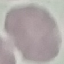

{
  "malaria_status": "uninfected",
  "image_type": "cell patch, automatically extracted from a larger field of view and resized to 64 × 64 pixels",
  "stain": "Giemsa",
  "capture": "smartphone through the microscope eyepiece",
  "preparation": "thin smear"
}